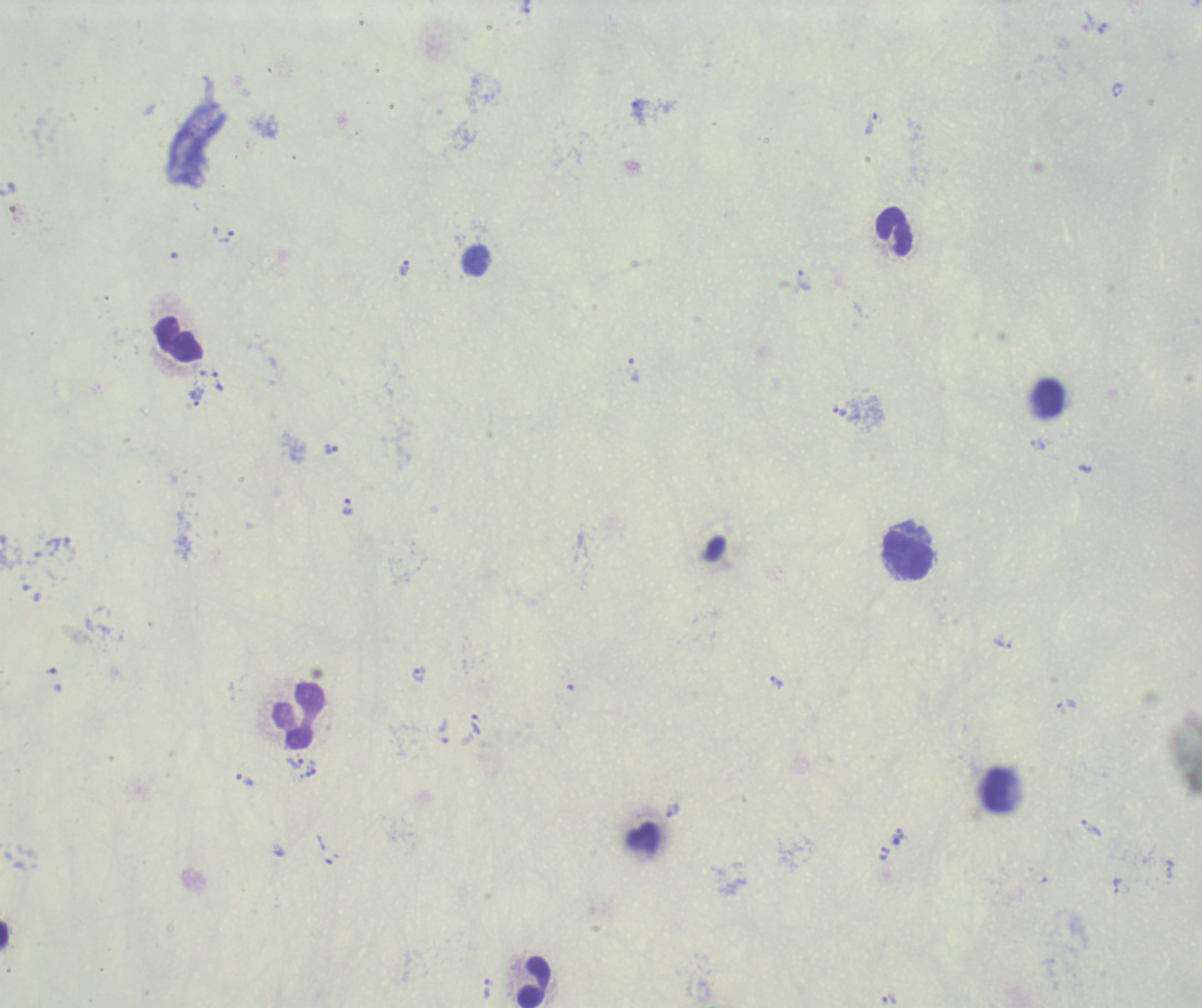
Approximate centers as [x, y] in pixels. Leukocyte locations: [894, 232], [476, 261], [179, 341], [1050, 398], [907, 555], [299, 714], [998, 789], [4, 935], [534, 982]. Trophozoite locations: [1101, 29], [1116, 90], [640, 112], [874, 123], [222, 235], [405, 268], [804, 281], [633, 369], [218, 382], [196, 397], [840, 412], [1037, 445], [332, 449], [1084, 468], [347, 507], [1002, 642], [419, 675], [776, 683], [1067, 705], [475, 726], [442, 731], [294, 763], [244, 780], [672, 810], [1090, 827], [898, 833], [884, 854], [1169, 868], [1117, 885], [486, 989], [888, 1000]. Romanowsky stain. Result: Plasmodium parasites identified. Previously used in an actual diagnosis. Background quality: poor. Captured at 100x magnification. Image is 1202×1008 pixels. Thick smear of blood. One field from this slide.